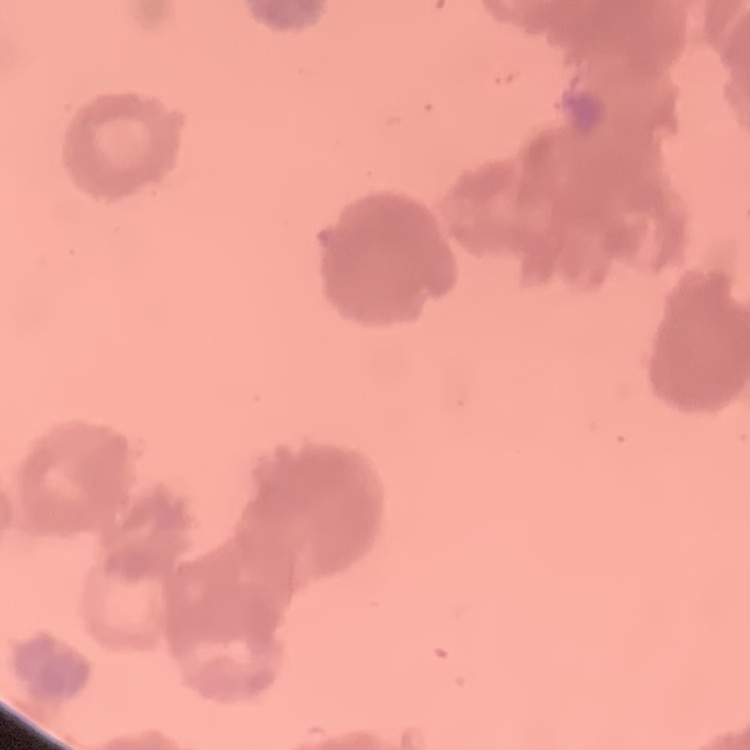
The red blood cells show rouleaux formation. Thin blood film. One tile cut from a larger photomicrograph. Stained with either Field's or Giemsa.